State the preparation type.
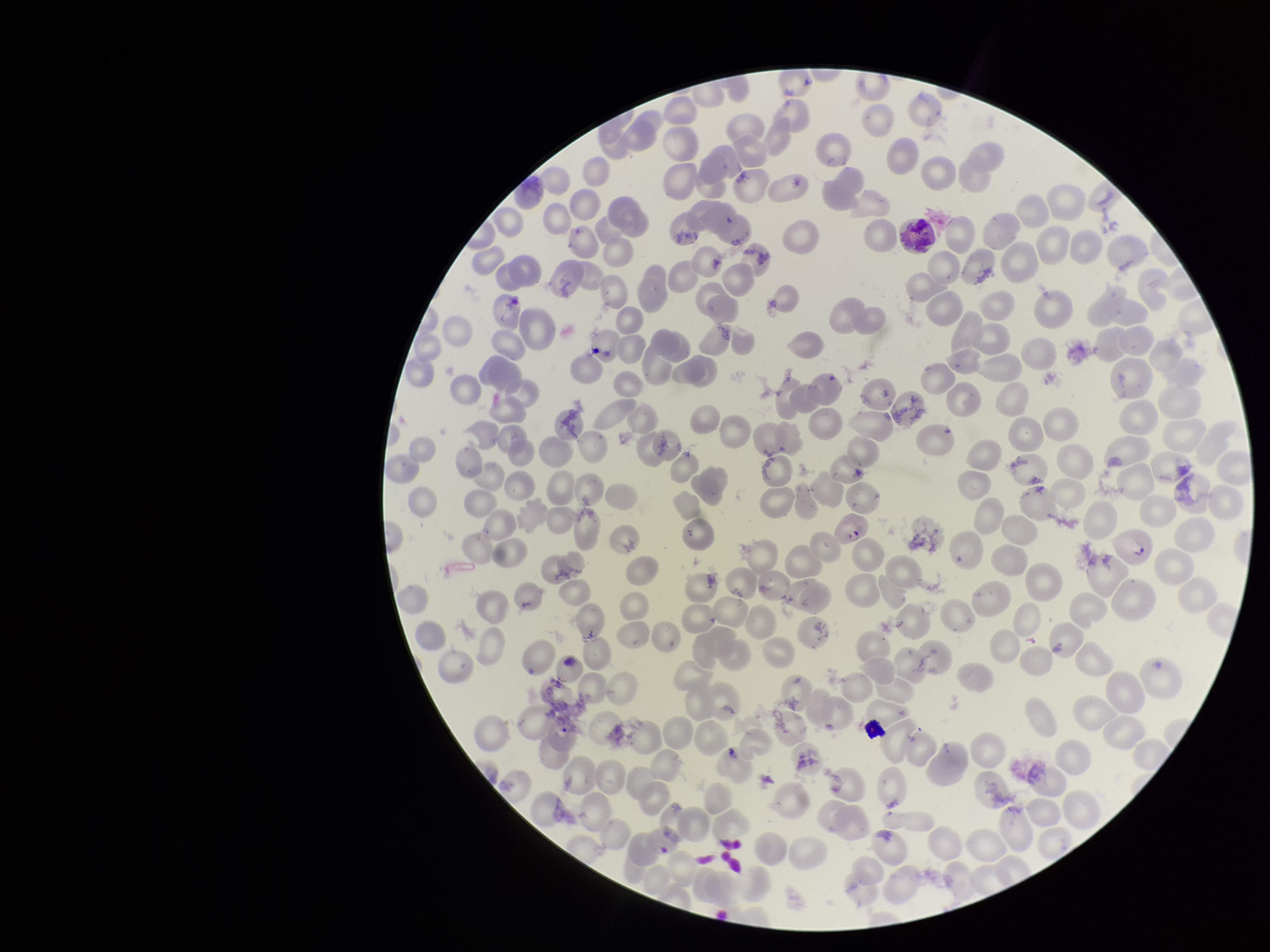

Thin.

parasitized red blood cells = identified
parasitized red blood cell count = 2
image size = 1270×952 pixels
patient malaria status = infected
species reported for this patient = Plasmodium falciparum
capture = smartphone photograph through the microscope eyepiece
red blood cell count = 228
stain = Giemsa
field of view = one from this slide